Assess this cell for malaria.
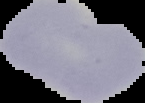
Uninfected.

Segmented cell region on a black background. Image is 145×103 pixels. From a thin blood film.